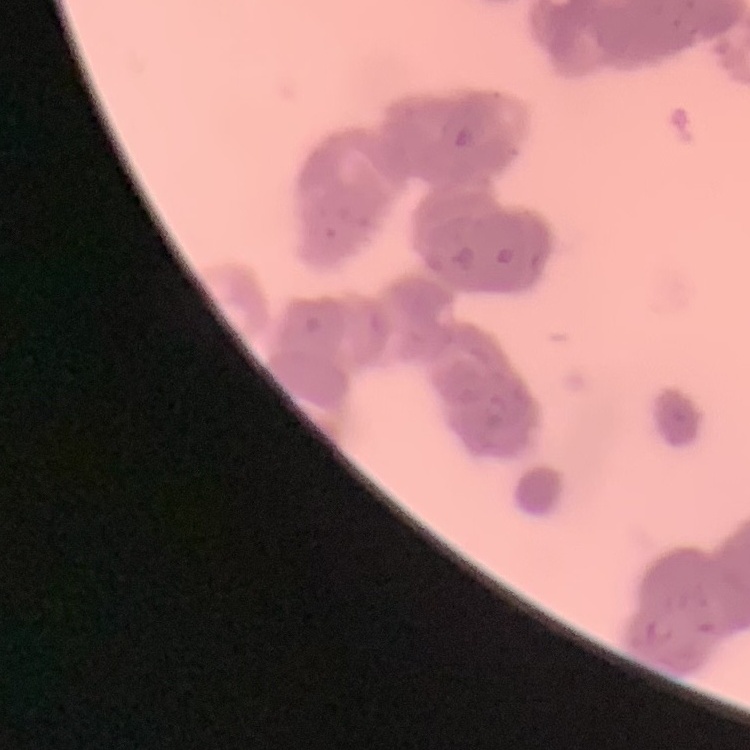 The red blood cells exhibit rouleaux formation. Field's or Giemsa stain. Thin blood film. Square crop of a larger photomicrograph.